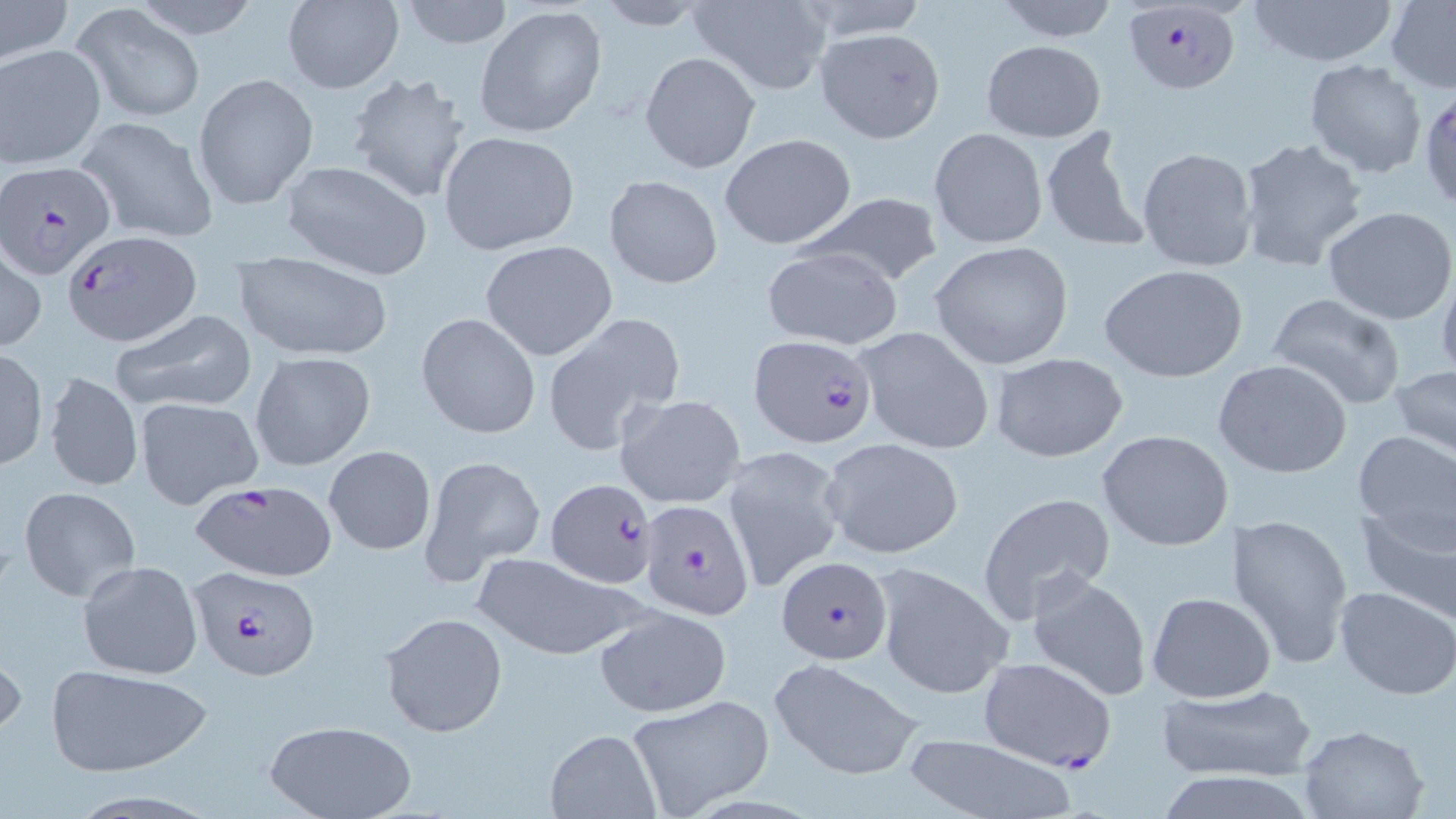

Summary:
  - Coordinate format: approximate bounding boxes as (x1, y1, x2, y2) in pixels
  - Uninfected red blood cell locations (subset): (394, 0, 516, 50), (590, 0, 716, 30), (989, 0, 1123, 43), (1244, 0, 1403, 68), (280, 1, 404, 93), (0, 2, 73, 62), (689, 2, 831, 92), (1386, 2, 1456, 90), (70, 4, 208, 123), (475, 5, 606, 139), (814, 29, 947, 144), (980, 39, 1106, 140), (0, 44, 105, 168), (640, 51, 760, 173), (1304, 59, 1427, 178), (345, 69, 473, 205), (193, 71, 319, 211), (74, 115, 220, 246), (1037, 123, 1154, 257), (928, 127, 1048, 249), (438, 129, 580, 256), (955, 130, 1119, 263), (719, 133, 858, 249), (1234, 137, 1369, 272), (1136, 146, 1257, 273), (277, 160, 435, 280), (603, 173, 723, 289), (793, 193, 944, 291), (1323, 205, 1456, 325), (480, 240, 617, 359), (929, 240, 1075, 369), (1, 245, 47, 353), (758, 246, 903, 350), (233, 254, 394, 362), (1099, 263, 1248, 382), (1437, 265, 1456, 385), (1265, 291, 1407, 411), (109, 308, 256, 414), (1226, 308, 1393, 461), (416, 312, 542, 438), (543, 316, 685, 455), (851, 326, 996, 456), (0, 347, 48, 470), (250, 350, 376, 470), (988, 351, 1129, 461), (1212, 357, 1354, 480), (1390, 365, 1456, 459), (44, 371, 142, 492), (614, 392, 747, 509), (135, 396, 263, 509), (1098, 429, 1236, 552), (1351, 431, 1455, 552), (819, 436, 964, 560), (323, 445, 436, 556), (724, 446, 847, 592), (418, 454, 546, 582), (18, 486, 140, 602), (976, 491, 1117, 624), (1353, 497, 1456, 621), (1228, 512, 1354, 669), (471, 552, 644, 658), (77, 560, 204, 680), (870, 561, 1015, 702), (1026, 572, 1154, 702), (1335, 586, 1456, 698), (1146, 591, 1276, 702), (593, 606, 732, 717), (378, 612, 506, 737), (0, 637, 24, 745), (768, 658, 926, 781), (44, 666, 211, 775), (1155, 684, 1317, 781), (626, 695, 775, 816), (260, 720, 417, 819), (1296, 723, 1430, 818), (545, 729, 660, 817), (902, 732, 1075, 819), (1153, 769, 1323, 818)
  - Plasmodium falciparum-infected red blood cell locations (subset): (1121, 3, 1242, 95), (2, 163, 115, 280), (65, 232, 201, 348), (748, 336, 878, 450), (187, 481, 339, 581), (640, 499, 756, 620), (775, 558, 892, 664), (188, 563, 322, 680), (977, 659, 1115, 767)
  - Slide-level diagnosis: Plasmodium falciparum
  - Image size: 1456×819 pixels
  - Modality: light microscopy
  - Magnification: 1000x
  - Stain: May-Grünwald-Giemsa
  - Field of view: single
  - Preparation: thin blood film